Assess this cell for malaria.
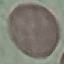
It is uninfected.

Cell patch, automatically extracted from a larger field of view and resized to 64 × 64 pixels. Thin blood smear. Acquired by smartphone through the microscope eyepiece. Giemsa stain.